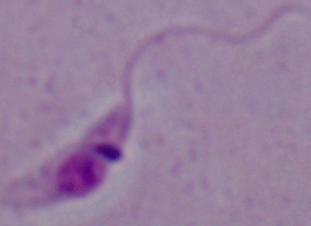
{
  "magnification": "1000x",
  "modality": "micrograph",
  "identification": "Leishmania"
}